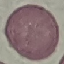
Summary:
  - Malaria status: uninfected
  - Capture: smartphone through the microscope eyepiece
  - Stain: Giemsa
  - Image type: automatically extracted cell patch, resized to 64 × 64 pixels
  - Preparation: thin blood film